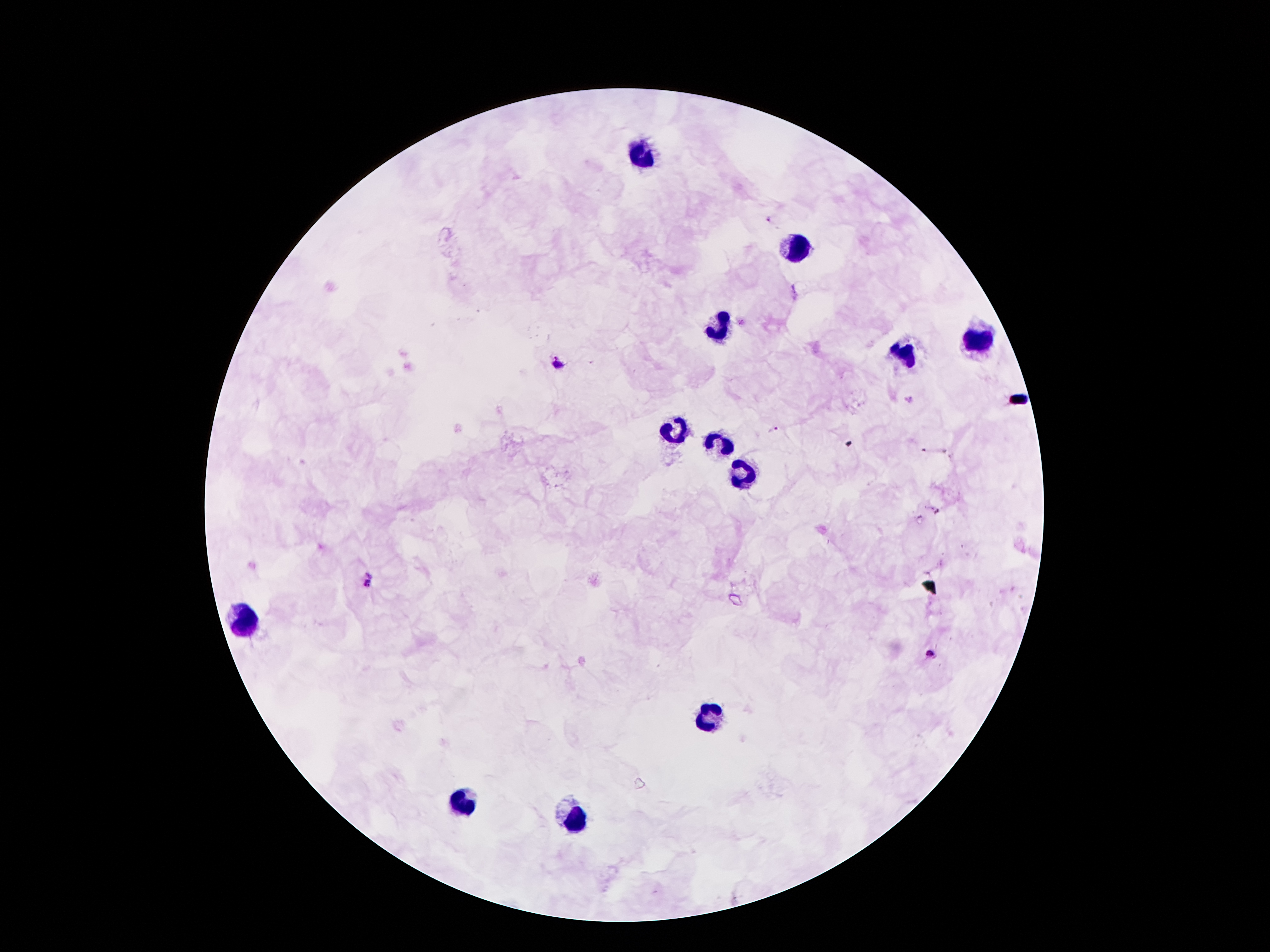

coordinate format = approximate centers as [x, y] in pixels
Plasmodium parasite locations = [560, 363], [910, 399], [775, 428], [936, 510], [371, 581], [931, 652]
leukocyte locations = [645, 155], [798, 246], [725, 328], [979, 341], [904, 354], [674, 432], [718, 445], [740, 474], [243, 617], [705, 717], [466, 801], [574, 819]
capture = smartphone camera through the microscope eyepiece
preparation = thick blood film
field of view = one from this slide
stain = Giemsa
patient malaria status = infected with Plasmodium falciparum
magnification = 100x
image size = 1270×952 pixels